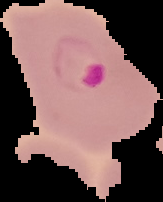 Image is 163×202 pixels. Malaria status: parasitized. From a thin blood smear. The area outside the segmented cell region is set to black.